Locate and identify every blood parasite.
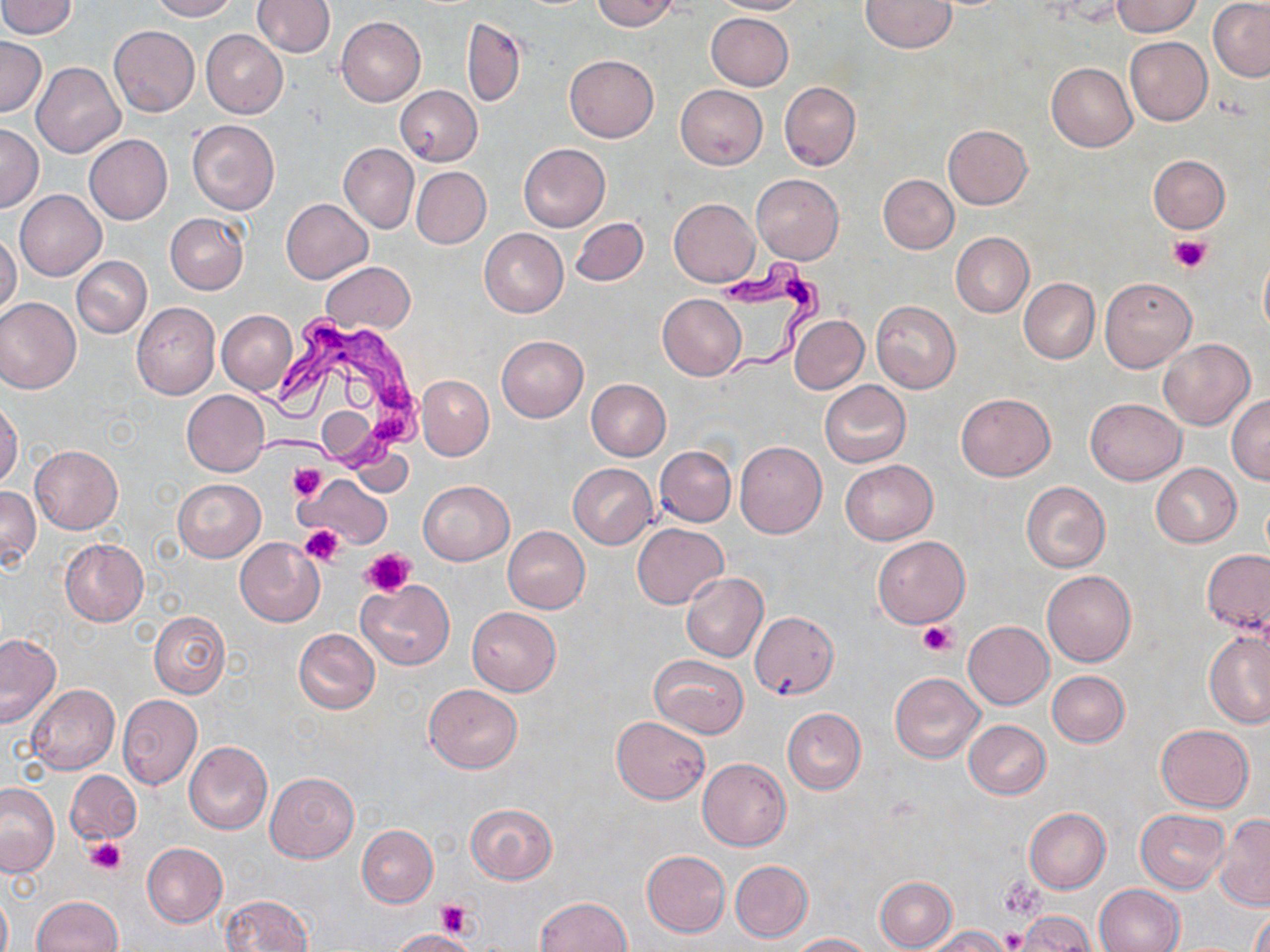
Approximate bounding boxes as (x1,y1)-(x2,y2) corner pairs in pixels.
Trypanosoma brucei: (715,250)-(831,383), (248,315)-(426,482).
No Plasmodium falciparum, Plasmodium ovale, Plasmodium malariae, Plasmodium vivax, or Babesia divergens observed.

Summary:
  - Uninfected red blood cell locations: (149,0)-(236,21), (591,0)-(680,31), (712,0)-(805,15), (1,1)-(77,38), (253,1)-(335,57), (860,1)-(957,52), (1113,1)-(1202,37), (1208,1)-(1270,81), (706,13)-(793,91), (337,16)-(426,105), (462,18)-(525,106), (109,25)-(200,116), (201,30)-(288,118), (0,36)-(46,117), (1124,37)-(1212,125), (565,55)-(659,142), (31,62)-(124,158), (1046,62)-(1136,151), (780,81)-(860,171), (676,84)-(768,169), (394,85)-(483,166), (187,120)-(280,215), (1,124)-(42,212), (943,124)-(1033,209), (85,135)-(172,224), (518,142)-(610,232), (339,144)-(418,233), (1148,155)-(1229,233), (411,166)-(491,248), (751,174)-(844,263), (878,174)-(958,254), (15,189)-(105,280), (669,198)-(760,286), (281,199)-(373,283), (165,213)-(248,293), (571,217)-(647,286), (480,228)-(568,317), (0,231)-(21,318), (951,232)-(1034,317), (71,256)-(151,338), (322,263)-(415,334), (1099,276)-(1197,371), (1019,278)-(1098,363), (657,294)-(746,380), (0,296)-(81,394), (871,300)-(961,394), (131,302)-(220,399), (217,309)-(297,396), (790,315)-(868,394), (496,335)-(588,421), (1158,338)-(1254,430), (417,375)-(493,460), (586,379)-(671,460), (820,380)-(911,468), (182,391)-(269,476), (955,393)-(1055,481), (1228,395)-(1270,484), (1085,398)-(1186,484), (0,400)-(22,488), (735,441)-(826,538), (30,445)-(123,534), (655,446)-(736,527), (840,460)-(937,545), (1151,463)-(1241,547), (568,464)-(657,548), (301,473)-(390,546), (173,478)-(264,561), (418,480)-(513,565), (1021,481)-(1110,573), (0,485)-(40,569), (632,523)-(727,609), (502,527)-(590,613), (873,536)-(969,628), (59,538)-(147,626), (235,538)-(324,626), (1202,549)-(1269,636), (1041,570)-(1136,667), (681,573)-(768,662), (356,581)-(454,669), (467,607)-(561,695), (149,611)-(230,698), (749,611)-(837,701), (963,620)-(1054,709), (1204,628)-(1270,727), (294,629)-(380,712), (0,633)-(61,728), (651,655)-(748,738), (1047,670)-(1130,747), (890,672)-(986,763), (424,683)-(521,772), (26,684)-(120,774), (117,694)-(202,788), (782,708)-(865,794), (611,715)-(710,802), (963,719)-(1051,798), (1155,723)-(1254,811), (184,741)-(273,834), (697,758)-(791,851), (65,770)-(141,845), (265,772)-(358,862), (0,782)-(58,877), (466,802)-(556,884), (1025,808)-(1110,893), (1136,809)-(1230,892), (1214,816)-(1270,910), (357,825)-(438,907), (143,843)-(228,927), (642,851)-(730,936), (730,860)-(813,942), (875,876)-(957,951), (1094,883)-(1184,952), (0,892)-(11,952), (221,894)-(314,952), (30,896)-(122,952), (535,896)-(631,952), (1250,909)-(1270,952), (1017,911)-(1095,951), (928,926)-(1009,952), (389,929)-(477,952), (790,933)-(875,951)
  - Platelet locations: (1168,232)-(1213,274), (288,462)-(327,502), (299,525)-(344,565), (361,547)-(415,598), (916,620)-(956,656), (87,836)-(125,873), (1000,877)-(1046,920), (435,899)-(473,940), (1000,928)-(1027,950)
  - Slide-level diagnosis: Trypanosoma brucei
  - Field of view: one of a larger specimen
  - Modality: optical microscopy
  - Image size: 1270×952 pixels
  - Preparation: thin blood smear
  - Stain: May-Grünwald-Giemsa
  - Magnification: 1000x